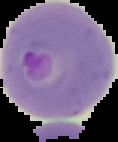

Result: malaria parasites detected. From a thin blood film. Image is 118×142 pixels. Segmented cell region on a black background.